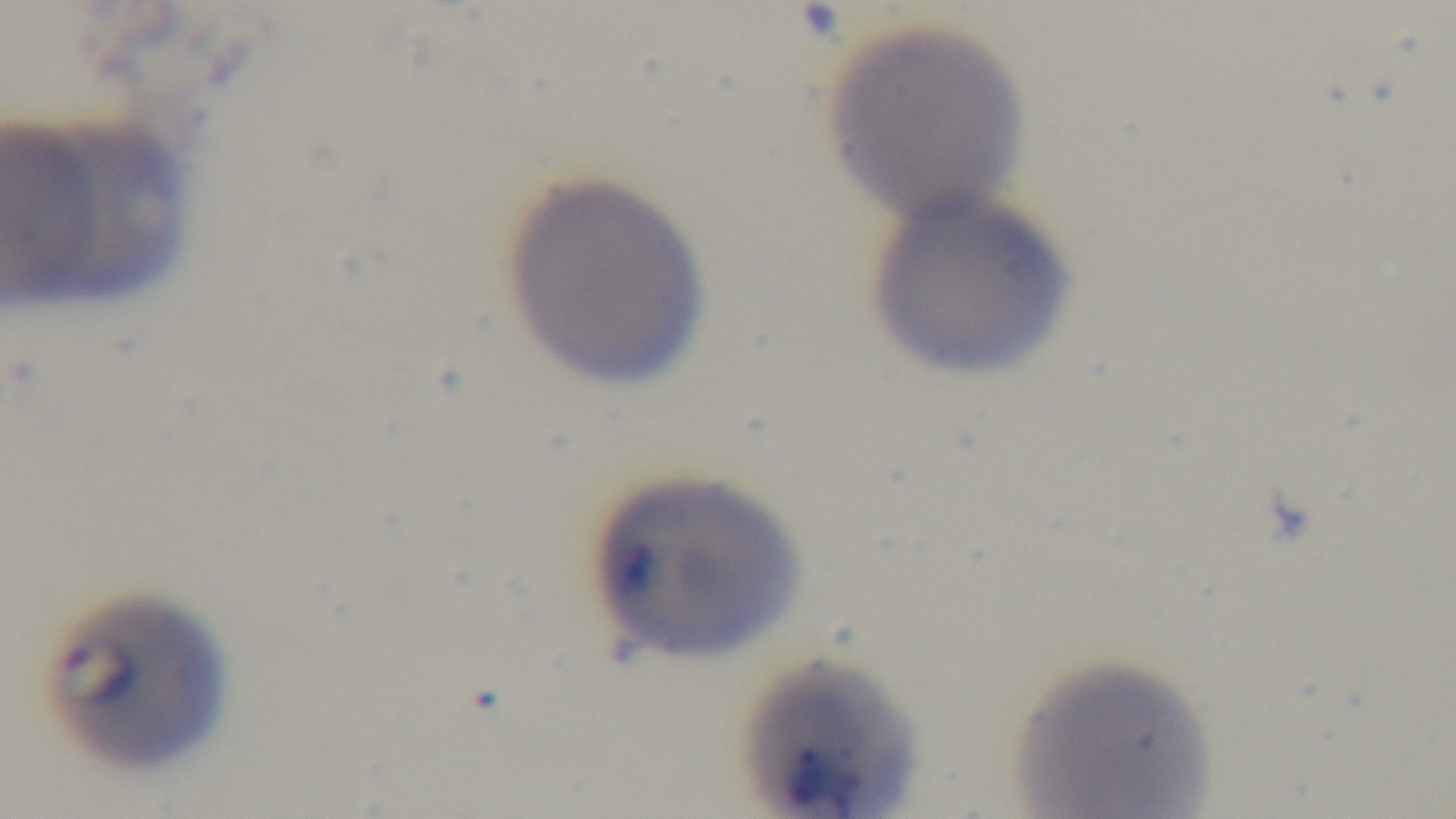

Summary:
  - Capture: mounted 4K digital camera
  - Modality: light microscopy
  - Stain: Giemsa
  - Objective: 100x oil immersion
  - Preparation: thin
  - Malaria status: infected
  - Field of view: single